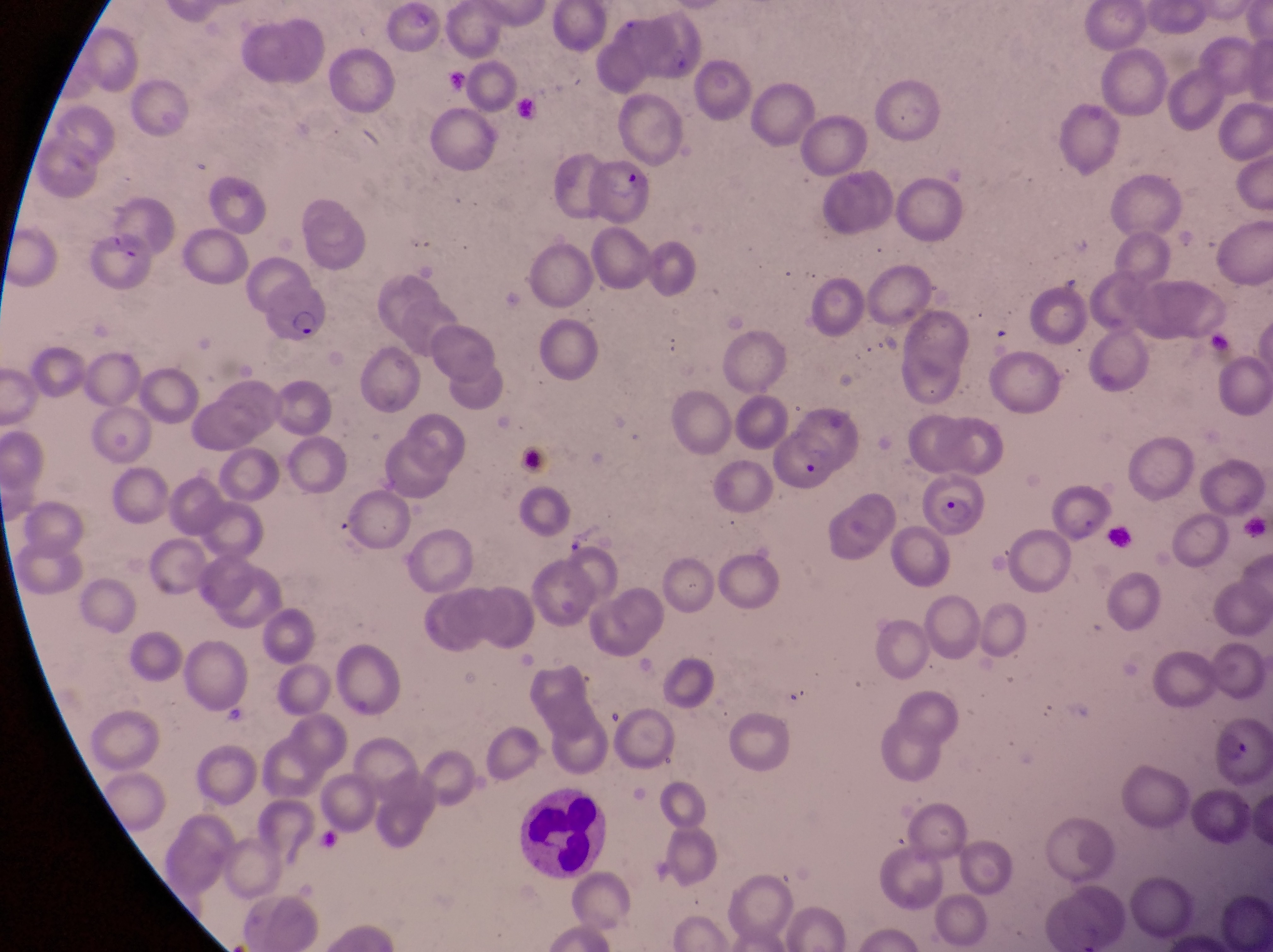
Approximate bounding boxes as {left, top, right, bottom} in pixels.
Summary:
  - Leukocyte locations: {516, 786, 609, 879}
  - Parasitised red blood cell locations: {582, 157, 660, 224}, {82, 232, 154, 297}, {255, 272, 335, 349}, {776, 424, 839, 496}, {928, 469, 986, 544}, {1211, 712, 1271, 789}
  - Trophozoite locations: {561, 524, 594, 556}
  - Magnification: 1000x
  - Capture: smartphone photograph through the eyepiece of an Olympus CX-23 microscope
  - Image size: 1273×952 pixels
  - Country: Uganda
  - Preparation: thin blood smear
  - Field of view: single